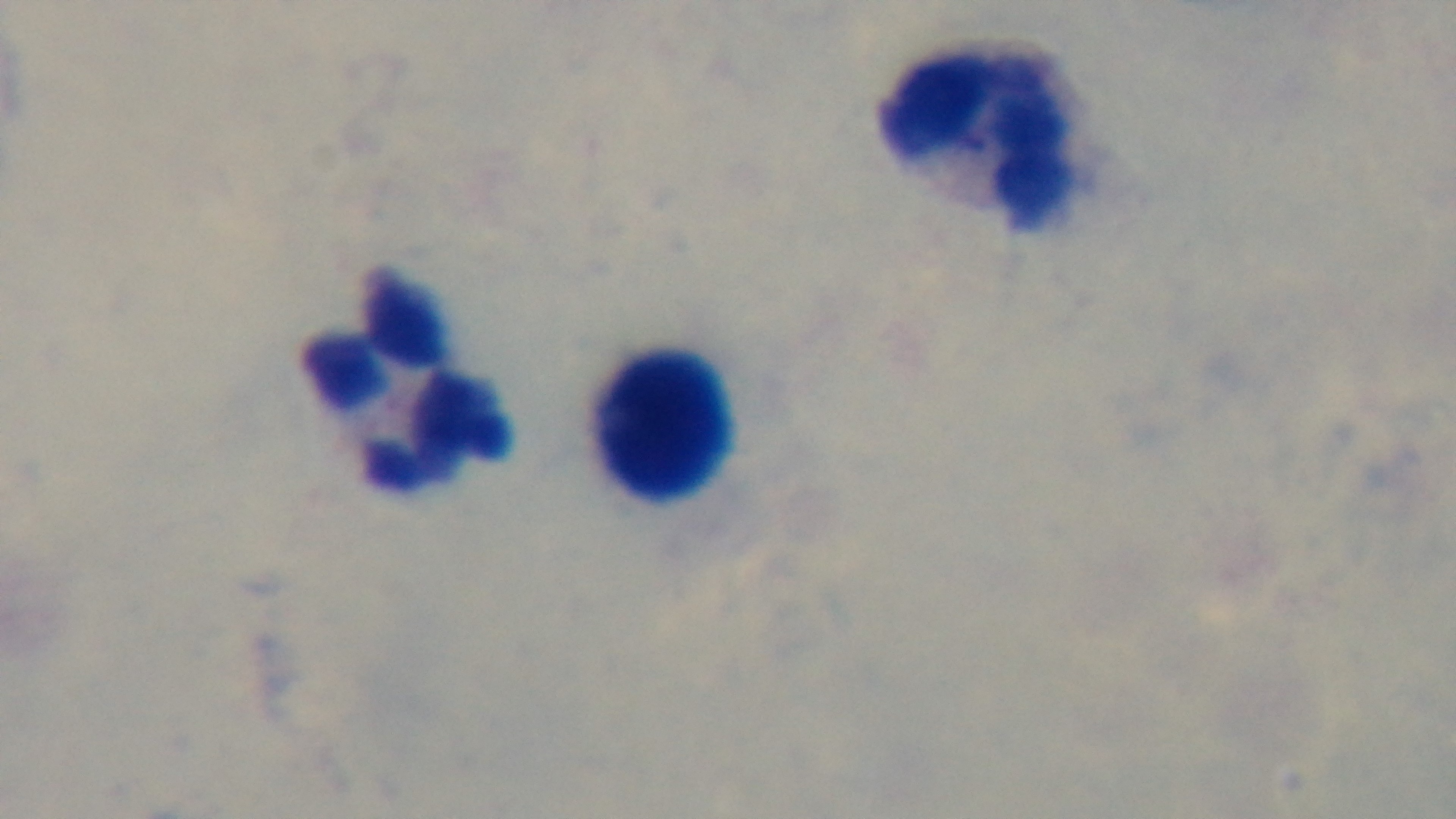

Summary:
  - Stain: Giemsa
  - Modality: light microscopy
  - Objective: 100x oil immersion
  - Preparation: thick
  - Malaria status: uninfected
  - Capture: mounted 4K digital camera
  - Field of view: one from the slide